Classify this cell by malaria status.
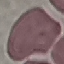

It is uninfected.

Automatically extracted cell patch, resized to 64 × 64 pixels. Giemsa stain. Thin blood smear. Photographed with a smartphone camera at the microscope eyepiece.